Give the position of every malaria parasite, noting whether each is a trophozoite, schizont, or gametocyte.
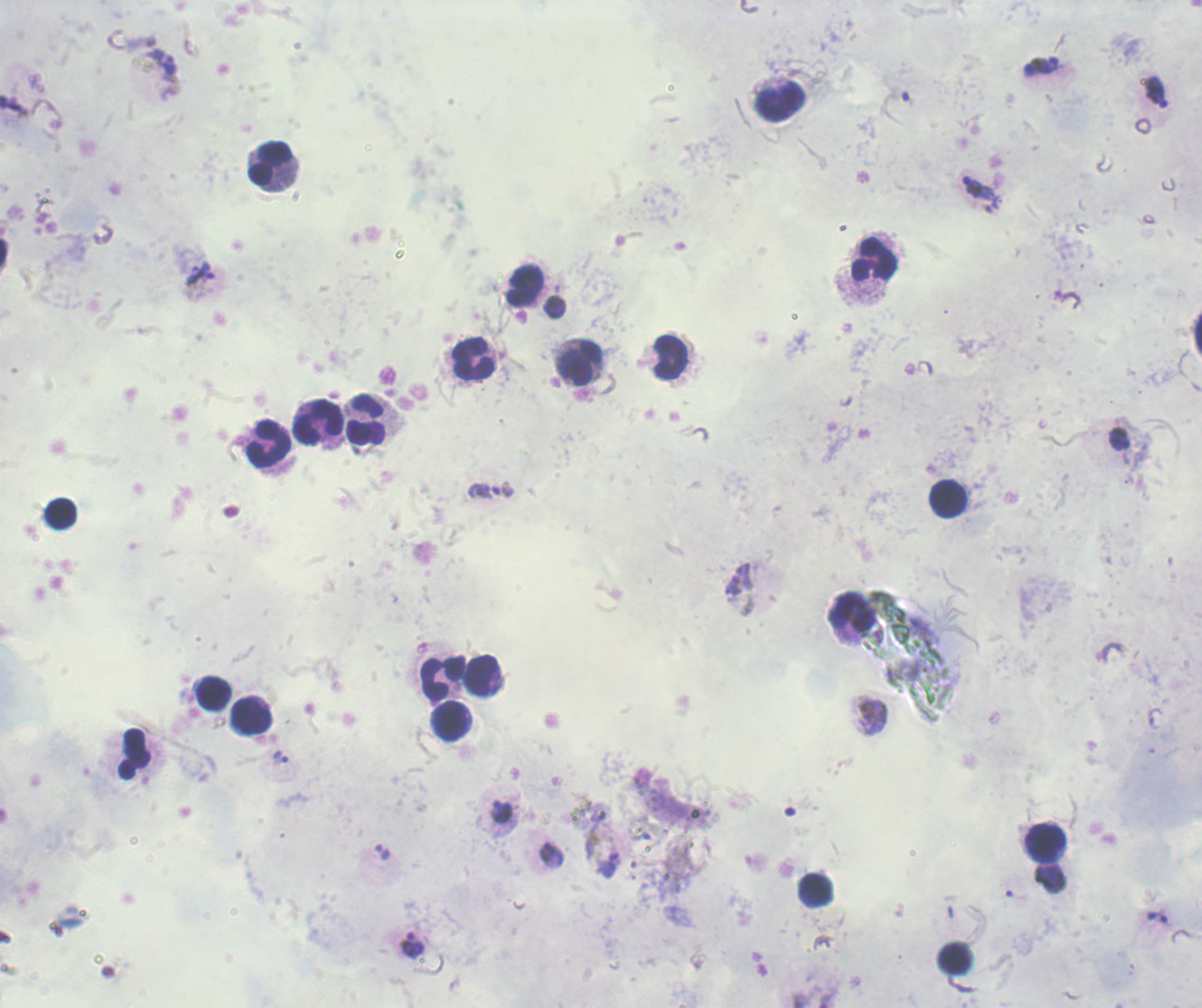
Approximate centers as [x, y] in pixels.
Trophozoites: [163, 62], [1041, 65], [1156, 93], [979, 188], [199, 272], [1119, 440], [503, 488], [736, 579], [870, 715], [281, 758], [501, 811], [382, 852], [551, 854], [610, 866], [1158, 918], [413, 944].
No schizont or gametocyte forms observed.

Approximate centers as [x, y] in pixels.
Summary:
  - Leukocyte locations: [779, 101], [272, 165], [873, 258], [525, 284], [669, 358], [473, 359], [581, 362], [366, 420], [319, 423], [269, 445], [948, 498], [61, 513], [849, 610], [485, 675], [443, 678], [212, 694], [252, 715], [450, 721], [133, 753], [1045, 844], [815, 891], [955, 958]
  - Background quality: unsatisfactory
  - Context: previously used in a real diagnosis
  - Preparation: thick blood film
  - Field of view: single
  - Stain: Romanowsky
  - Magnification: 100x
  - Image size: 1202×1008 pixels